Locate every leukocyte (white blood cell).
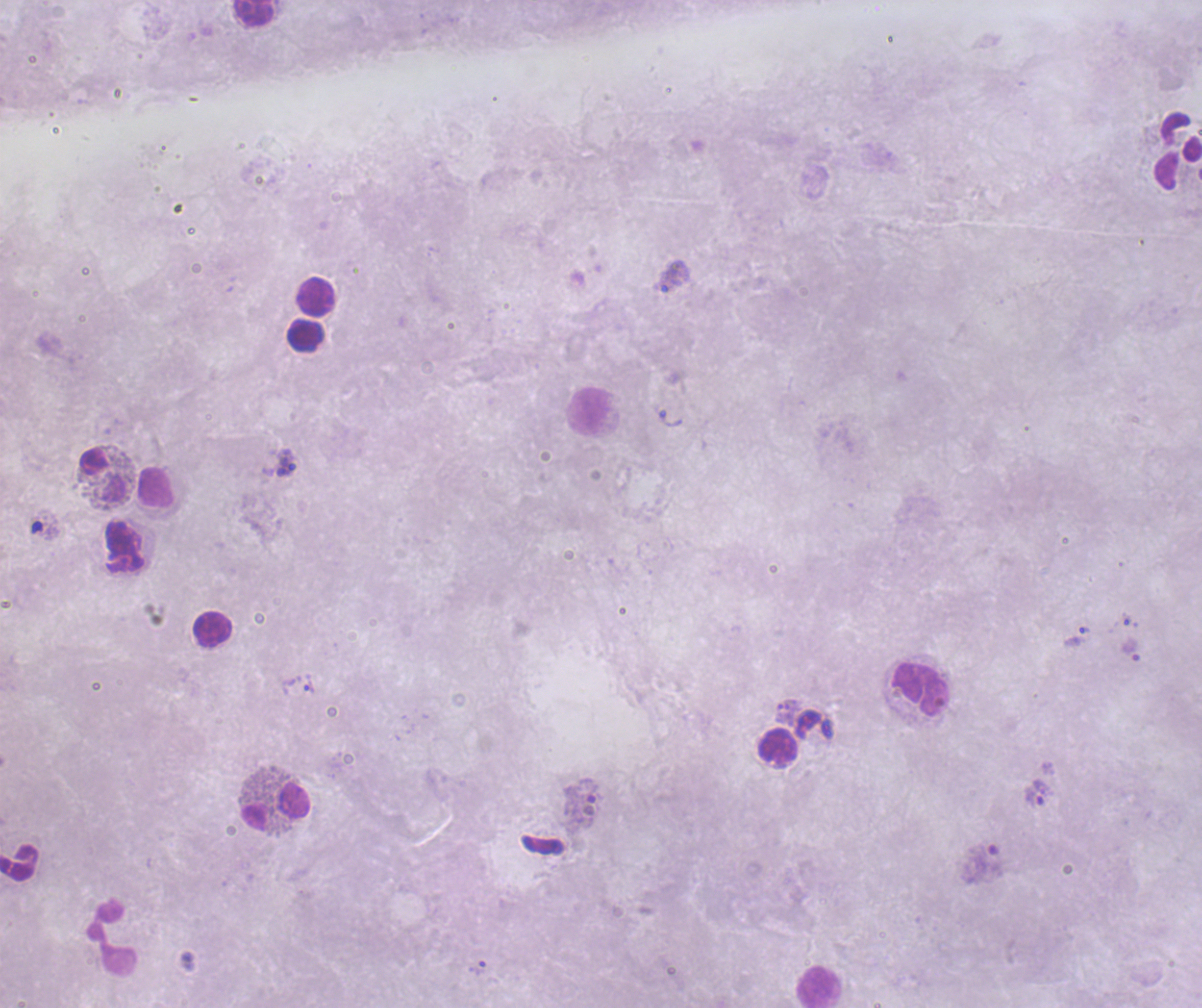

Approximate object centers, in pixels from the top-left corner.
Leukocytes: (x=253, y=13), (x=1178, y=150), (x=316, y=296), (x=306, y=335), (x=589, y=411), (x=103, y=475), (x=155, y=486), (x=124, y=548), (x=212, y=629), (x=921, y=689), (x=778, y=747), (x=276, y=806), (x=19, y=863), (x=111, y=940), (x=820, y=988).

Approximate object centers, in pixels from the top-left corner.
Summary:
  - Trophozoite locations: (x=675, y=277), (x=670, y=418), (x=287, y=463), (x=1075, y=637), (x=308, y=684), (x=785, y=711), (x=1037, y=794), (x=477, y=968)
  - Preparation: thick blood film
  - Magnification: 100x
  - Coloration quality: bad
  - Result: positive for malaria parasites
  - Stain: Romanowsky
  - Context: previously used in a real diagnosis
  - Field of view: one from this slide
  - Image size: 1202×1008 pixels
  - Background quality: unsatisfactory